Locate every Plasmodium parasite.
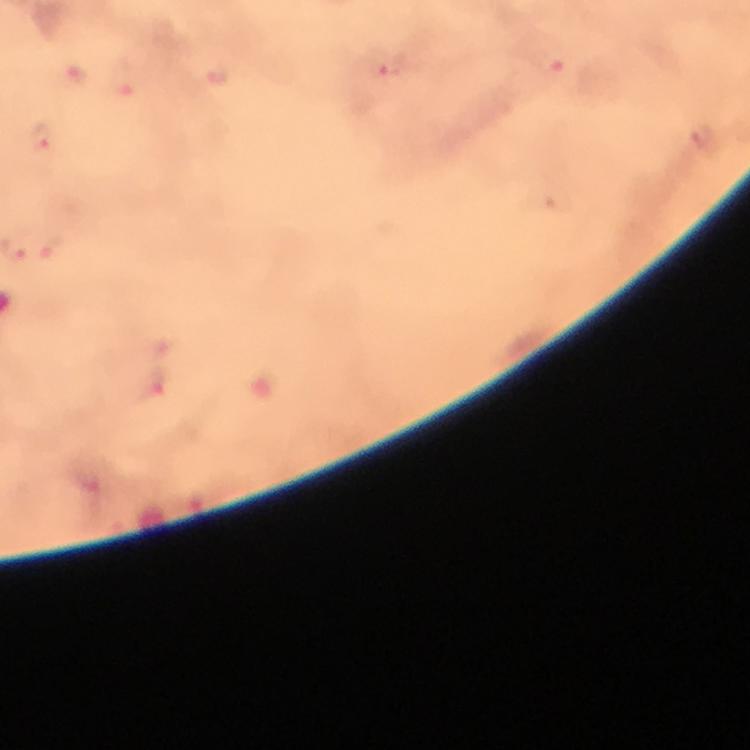
Approximate centers as [x, y] in pixels.
Plasmodium parasites: [396, 65], [553, 71], [42, 137], [51, 246], [154, 386].

Summary:
  - Capture: smartphone photograph through a microscope
  - Preparation: thick blood film
  - Magnification: 100x
  - Image size: 750×750 pixels
  - Immersion oil: used
  - Stain: Giemsa
  - Cropped from: a single field of view
  - Context: from a diagnostic examination for malaria